Locate every malaria parasite.
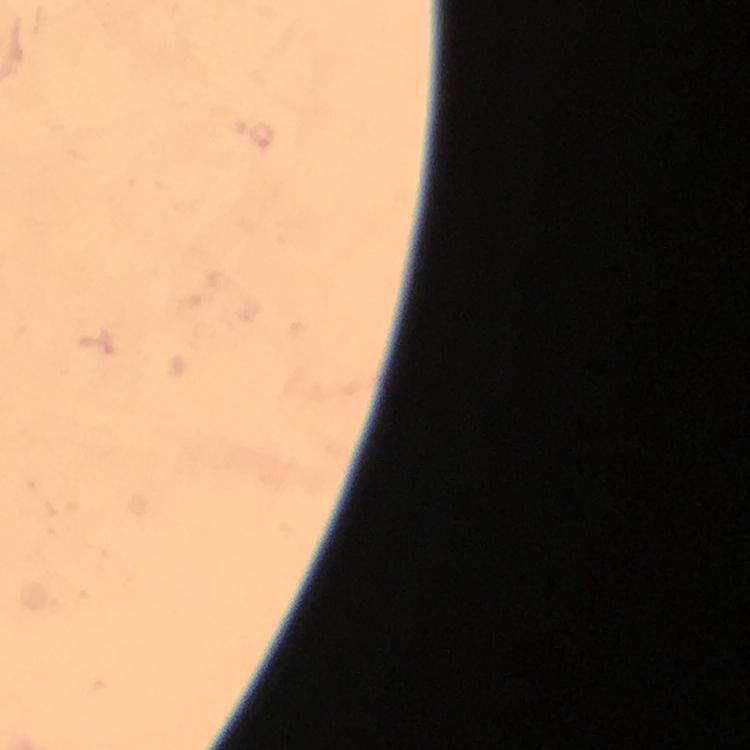

Approximate centers as (x, y) in pixels.
Malaria parasites: (260, 134).

Image is 750×750 pixels. Cropped region of a single field of view. From a diagnostic examination for malaria. Thick smear. Smartphone photograph taken through a microscope. 100x magnification. Immersion oil was used. Giemsa stain.